Locate and identify every blood parasite.
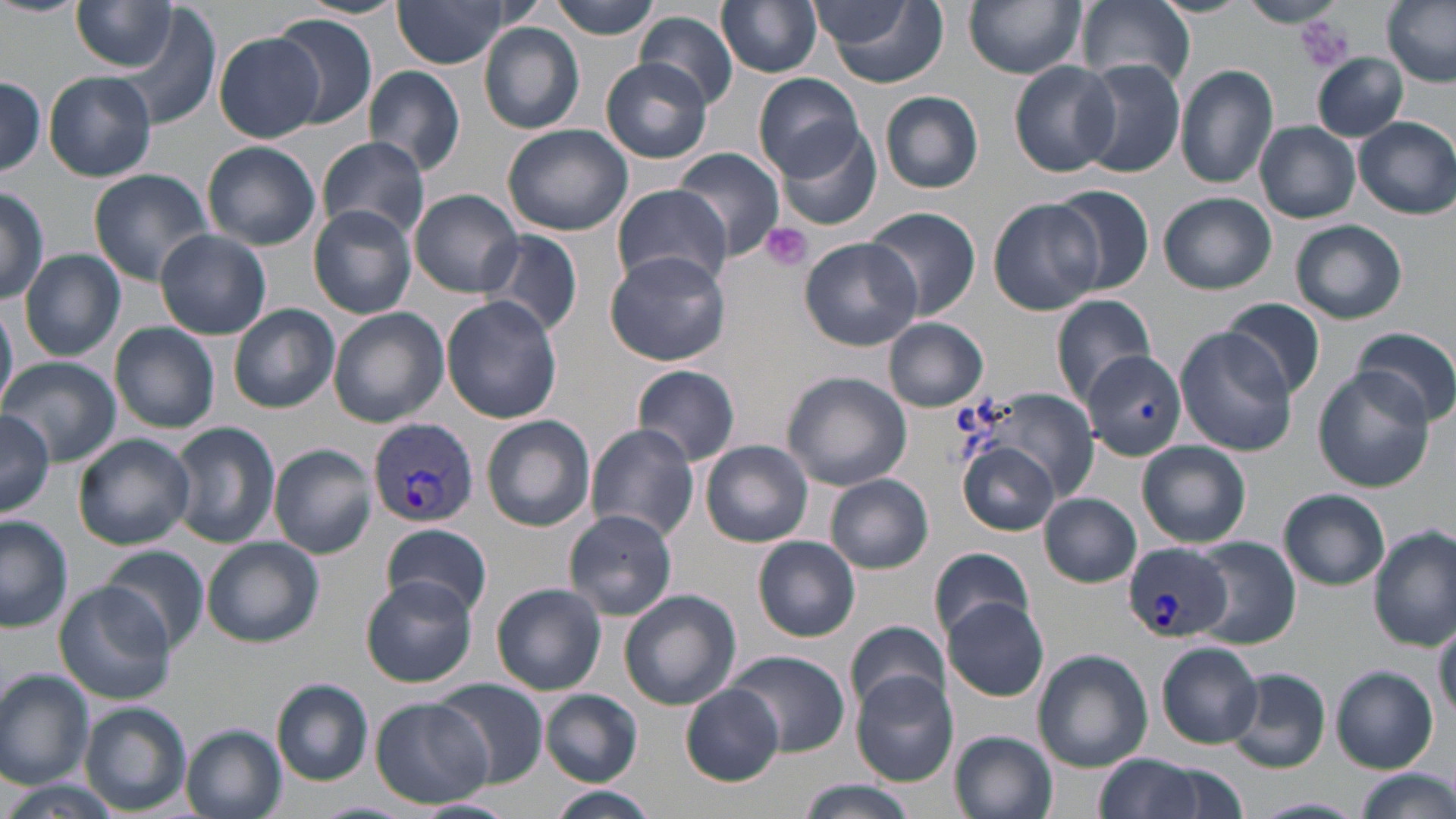

Approximate bounding boxes as named x1/y1/x2/y2 corners in pixels.
Plasmodium vivax-infected red blood cells: (x1=367, y1=418, x2=479, y2=527), (x1=1123, y1=544, x2=1231, y2=643).
No Plasmodium falciparum, Plasmodium ovale, Plasmodium malariae, Babesia divergens, or Trypanosoma brucei observed.

Uninfected red blood cell locations: (x1=0, y1=0, x2=86, y2=18), (x1=299, y1=0, x2=409, y2=19), (x1=393, y1=0, x2=515, y2=68), (x1=548, y1=0, x2=664, y2=38), (x1=716, y1=0, x2=823, y2=77), (x1=964, y1=0, x2=1086, y2=78), (x1=1078, y1=0, x2=1193, y2=90), (x1=1241, y1=0, x2=1340, y2=27), (x1=1382, y1=0, x2=1456, y2=87), (x1=817, y1=1, x2=947, y2=88), (x1=72, y1=2, x2=180, y2=72), (x1=811, y1=2, x2=921, y2=51), (x1=271, y1=14, x2=380, y2=129), (x1=637, y1=14, x2=737, y2=109), (x1=479, y1=24, x2=585, y2=134), (x1=214, y1=31, x2=323, y2=142), (x1=1313, y1=53, x2=1407, y2=140), (x1=601, y1=57, x2=712, y2=164), (x1=1079, y1=59, x2=1186, y2=180), (x1=1008, y1=61, x2=1120, y2=178), (x1=364, y1=65, x2=465, y2=176), (x1=1175, y1=65, x2=1278, y2=189), (x1=45, y1=71, x2=157, y2=182), (x1=754, y1=74, x2=865, y2=181), (x1=0, y1=77, x2=47, y2=179), (x1=881, y1=90, x2=984, y2=194), (x1=1354, y1=116, x2=1456, y2=220), (x1=1256, y1=121, x2=1360, y2=223), (x1=503, y1=123, x2=633, y2=237), (x1=776, y1=125, x2=881, y2=232), (x1=315, y1=136, x2=431, y2=243), (x1=202, y1=141, x2=320, y2=251), (x1=671, y1=148, x2=787, y2=262), (x1=87, y1=169, x2=213, y2=285), (x1=0, y1=184, x2=48, y2=307), (x1=610, y1=184, x2=733, y2=291), (x1=1050, y1=184, x2=1155, y2=295), (x1=412, y1=189, x2=524, y2=297), (x1=1158, y1=192, x2=1276, y2=294), (x1=988, y1=197, x2=1103, y2=314), (x1=307, y1=204, x2=417, y2=319), (x1=864, y1=206, x2=980, y2=320), (x1=1290, y1=219, x2=1408, y2=324), (x1=482, y1=229, x2=582, y2=339), (x1=155, y1=230, x2=271, y2=339), (x1=801, y1=236, x2=920, y2=349), (x1=604, y1=248, x2=730, y2=366), (x1=19, y1=250, x2=125, y2=360), (x1=1050, y1=293, x2=1156, y2=406), (x1=440, y1=297, x2=563, y2=424), (x1=1218, y1=298, x2=1325, y2=400), (x1=0, y1=299, x2=16, y2=413), (x1=228, y1=304, x2=339, y2=413), (x1=328, y1=308, x2=449, y2=428), (x1=884, y1=318, x2=988, y2=412), (x1=111, y1=322, x2=220, y2=433), (x1=1176, y1=327, x2=1297, y2=455), (x1=1355, y1=327, x2=1456, y2=427), (x1=1080, y1=348, x2=1185, y2=462), (x1=4, y1=357, x2=119, y2=464), (x1=633, y1=365, x2=741, y2=467), (x1=1314, y1=368, x2=1435, y2=491), (x1=781, y1=372, x2=913, y2=492), (x1=986, y1=391, x2=1096, y2=495), (x1=0, y1=409, x2=56, y2=520), (x1=480, y1=414, x2=595, y2=532), (x1=169, y1=422, x2=279, y2=548), (x1=586, y1=424, x2=699, y2=541), (x1=74, y1=432, x2=192, y2=549), (x1=701, y1=440, x2=814, y2=547), (x1=1138, y1=441, x2=1251, y2=547), (x1=960, y1=443, x2=1060, y2=536), (x1=270, y1=444, x2=376, y2=559), (x1=825, y1=476, x2=933, y2=573), (x1=1278, y1=489, x2=1391, y2=590), (x1=1041, y1=493, x2=1140, y2=587), (x1=563, y1=509, x2=678, y2=622), (x1=0, y1=517, x2=73, y2=633), (x1=382, y1=523, x2=492, y2=619), (x1=1372, y1=528, x2=1454, y2=649), (x1=753, y1=536, x2=861, y2=641), (x1=1189, y1=536, x2=1301, y2=650), (x1=201, y1=537, x2=324, y2=648), (x1=102, y1=547, x2=209, y2=653), (x1=929, y1=548, x2=1039, y2=642), (x1=362, y1=576, x2=477, y2=687), (x1=53, y1=582, x2=177, y2=704), (x1=491, y1=584, x2=606, y2=696), (x1=619, y1=589, x2=742, y2=713), (x1=941, y1=598, x2=1050, y2=702), (x1=1433, y1=622, x2=1456, y2=720), (x1=844, y1=625, x2=950, y2=713), (x1=1155, y1=641, x2=1263, y2=748), (x1=1033, y1=650, x2=1153, y2=772), (x1=727, y1=651, x2=849, y2=755), (x1=1331, y1=667, x2=1438, y2=771), (x1=1228, y1=668, x2=1330, y2=773), (x1=0, y1=672, x2=94, y2=790), (x1=850, y1=672, x2=956, y2=784), (x1=272, y1=680, x2=373, y2=785), (x1=435, y1=680, x2=547, y2=787), (x1=681, y1=684, x2=785, y2=786), (x1=540, y1=690, x2=642, y2=785), (x1=370, y1=698, x2=492, y2=808), (x1=79, y1=703, x2=190, y2=814), (x1=182, y1=725, x2=287, y2=819), (x1=952, y1=731, x2=1057, y2=818), (x1=1093, y1=754, x2=1214, y2=819), (x1=1350, y1=769, x2=1455, y2=819), (x1=796, y1=779, x2=919, y2=819), (x1=7, y1=780, x2=115, y2=819), (x1=546, y1=786, x2=659, y2=819), (x1=1249, y1=796, x2=1366, y2=817), (x1=415, y1=798, x2=516, y2=818). Platelet locations: (x1=1298, y1=15, x2=1354, y2=72), (x1=758, y1=223, x2=813, y2=272). Slide-level diagnosis: Plasmodium vivax. One field of a larger specimen. 1000x magnification. Thin blood smear. May-Grünwald-Giemsa-stained preparation. Optical microscopy. Image is 1456×819 pixels.